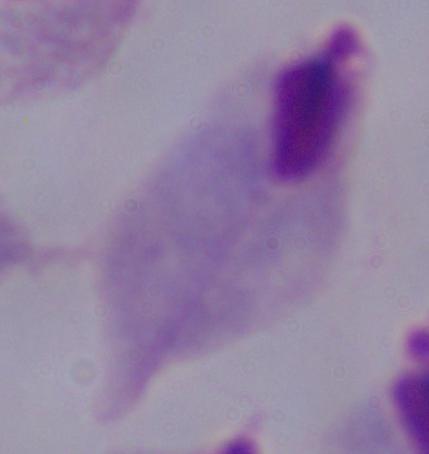
Summary:
  - Identification: trichomonad
  - Magnification: 1000x
  - Modality: micrograph